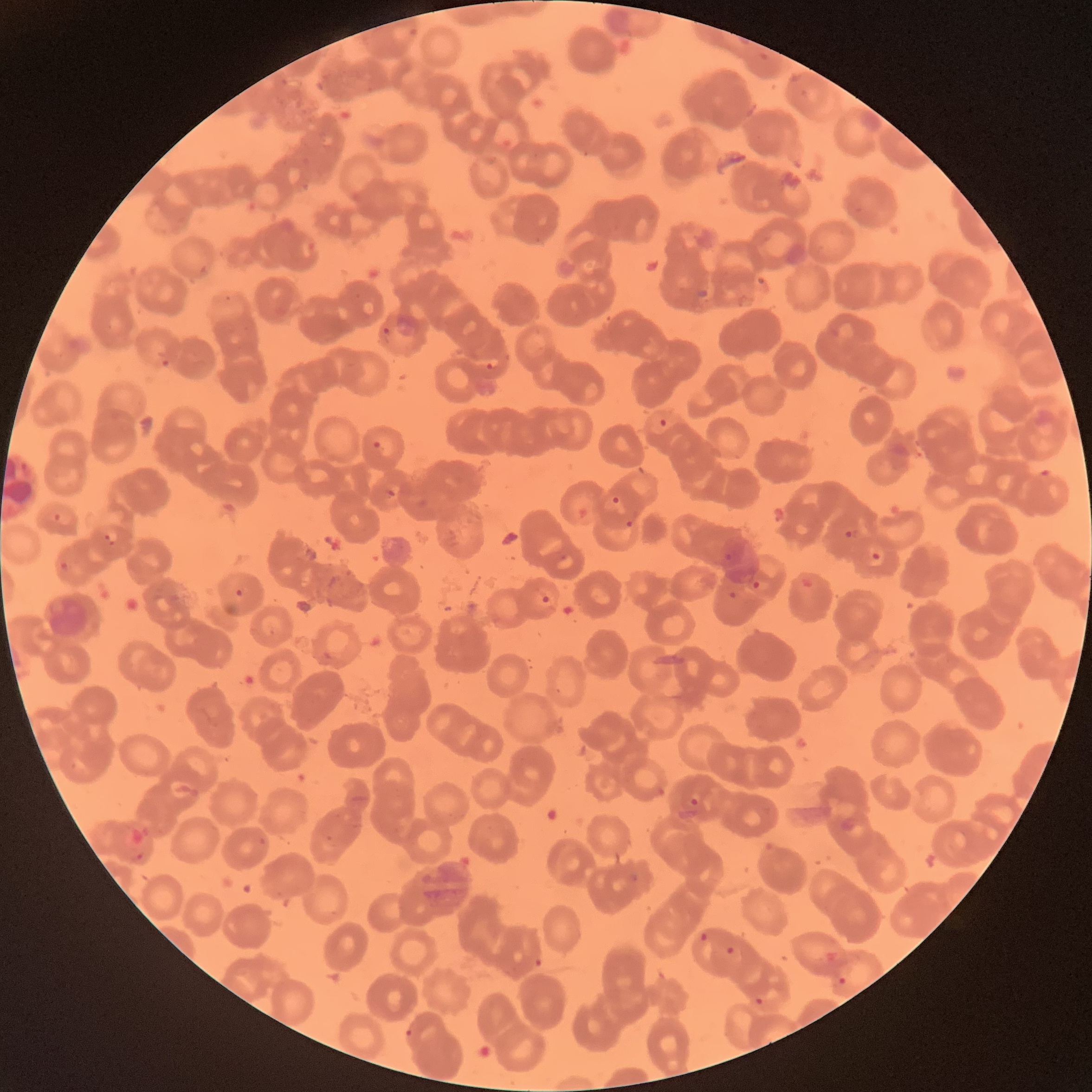
coordinate format = approximate bounding boxes as (x1,y1)-(x2,y2) corner pairs in pixels
Plasmodium parasites too small for a box (approximate centers as (x,y) in pixels) = (164,363)
Plasmodium parasite locations = (382,326)-(391,335), (485,360)-(494,370), (659,417)-(667,427), (373,440)-(382,450), (1039,469)-(1053,478), (386,488)-(396,497), (611,496)-(620,505), (625,520)-(634,528), (844,529)-(862,539), (102,531)-(122,547), (871,551)-(882,562), (59,560)-(70,571), (752,579)-(761,591), (234,588)-(244,597), (728,591)-(738,600), (541,595)-(550,604), (690,797)-(699,806), (136,851)-(146,862), (699,932)-(708,942), (725,945)-(736,956), (533,957)-(542,968), (837,977)-(847,986), (754,997)-(765,1007), (405,1028)-(415,1039)
image size = 1092×1092 pixels
red blood cell morphology = rouleaux formation
modality = optical microscopy
preparation = thin blood smear